Assess this cell for malaria.
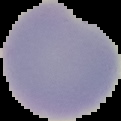

Uninfected.

Summary:
  - Image size: 121×121 pixels
  - Image type: segmented cell region with the area outside set to black
  - Preparation: thin blood film